Comment on the morphology of the red blood cells.
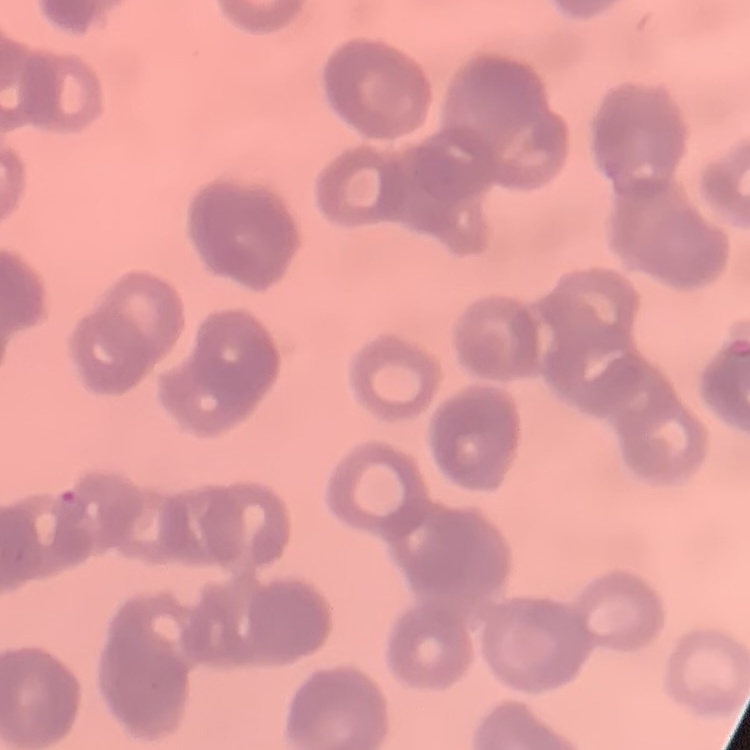
Rouleaux formation.

Summary:
  - Stain: Field's or Giemsa
  - Preparation: thin blood film
  - Image type: one tile cut from a larger photomicrograph